Report the malaria status of this cell.
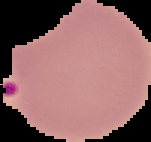
Uninfected.

Summary:
  - Image type: segmented cell region with the area outside set to black
  - Image size: 151×142 pixels
  - Preparation: thin blood smear